Name the parasite shown.
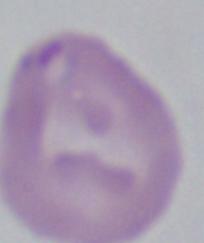
Babesia.

magnification = 1000x
modality = photomicrograph